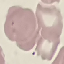 Malaria status: parasitized. Automatically extracted cell patch, resized to 64 × 64 pixels. Giemsa stain. Photographed with a smartphone camera at the microscope eyepiece. Thin smear of blood.